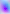

{
  "modality": "micrograph",
  "identification": "Toxoplasma gondii",
  "magnification": "400x"
}